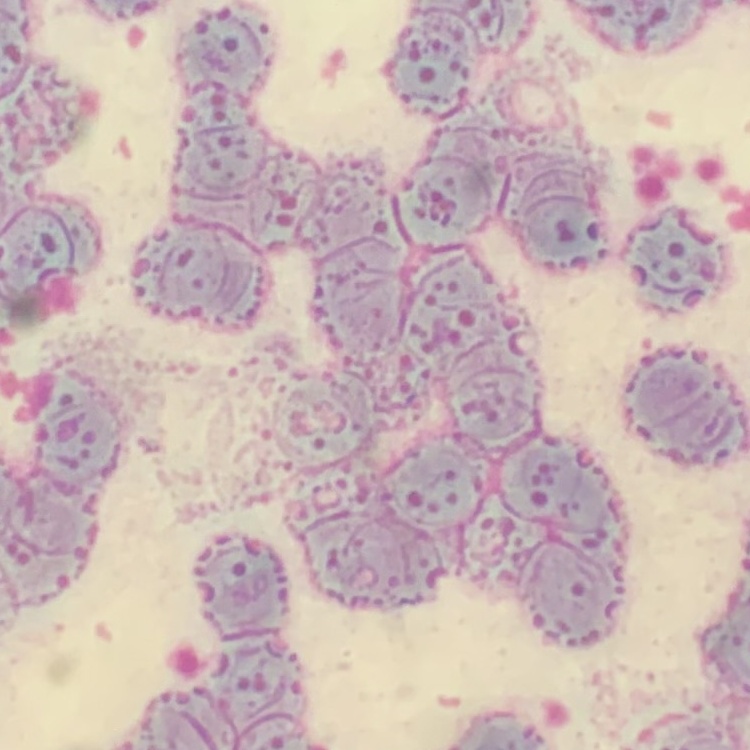
Summary:
  - Erythrocyte morphology: rouleaux formation
  - Preparation: thin blood smear
  - Stain: Field's or Giemsa
  - Image type: one tile cut from a larger photomicrograph